Outline each Plasmodium falciparum-infected red blood cell.
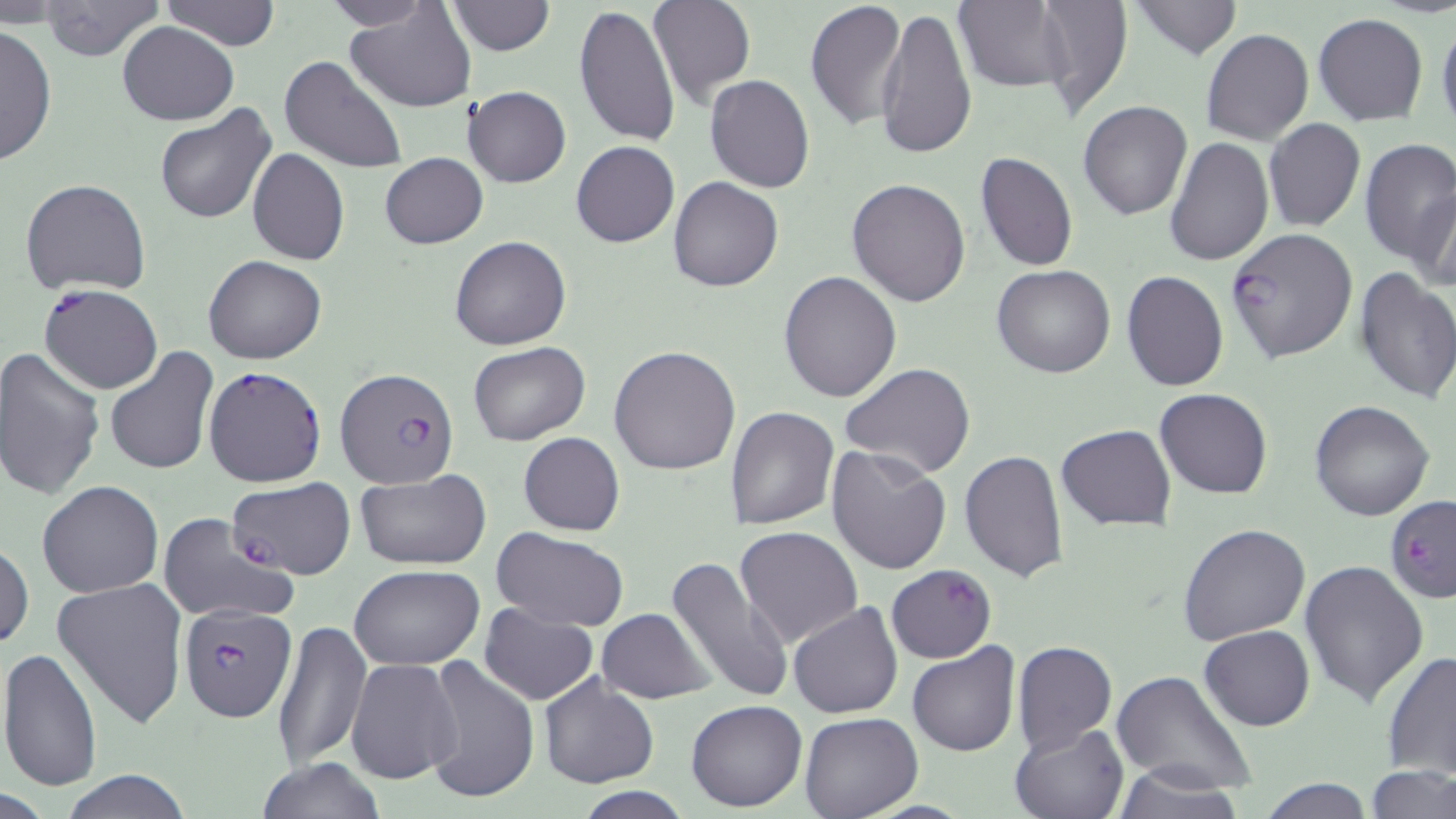

Approximate bounding boxes as (x1,y1)-(x2,y2) corner pairs in pixels.
Plasmodium falciparum-infected red blood cells: (1225,229)-(1358,364), (39,283)-(163,394), (203,367)-(326,486), (334,367)-(459,489), (228,476)-(355,582), (1384,495)-(1456,604), (887,565)-(997,663), (179,603)-(298,722).

slide_level_diagnosis: Plasmodium falciparum
image_size: 1456×819 pixels
stain: May-Grünwald-Giemsa
preparation: thin blood film
magnification: 1000x
uninfected_red_blood_cell_locations: 'approximate bounding boxes as (x1,y1)-(x2,y2) corner pairs in pixels: (160,0)-(281,50), (319,0)-(435,30), (803,0)-(908,131), (1035,0)-(1133,116), (1127,0)-(1243,60), (36,1)-(165,61), (446,1)-(555,55), (647,1)-(756,109), (343,2)-(477,113), (956,2)-(1073,92), (55,5)-(225,83), (574,5)-(680,147), (875,5)-(976,160), (1313,12)-(1428,125), (1437,20)-(1456,128), (117,21)-(238,125), (0,23)-(56,167), (1202,30)-(1313,144), (279,53)-(407,174), (706,75)-(815,192), (462,86)-(570,188), (1078,100)-(1193,220), (153,104)-(276,225), (1263,119)-(1365,233), (1163,136)-(1273,266), (1358,137)-(1455,265), (571,141)-(678,249), (247,148)-(348,265), (976,152)-(1077,273), (379,153)-(487,249), (668,176)-(784,292), (20,177)-(151,296), (845,177)-(972,307), (1414,182)-(1456,294), (449,237)-(571,351), (203,254)-(326,364), (991,265)-(1116,379), (1353,266)-(1456,404), (777,270)-(901,404), (1122,271)-(1228,391), (468,342)-(590,447), (103,346)-(220,475), (609,346)-(740,475), (0,348)-(105,500), (841,363)-(975,480), (1155,388)-(1272,498), (1309,399)-(1434,521), (725,407)-(840,531), (1057,425)-(1175,530), (518,432)-(624,535), (825,444)-(952,575), (958,449)-(1069,581), (354,471)-(491,568), (37,480)-(164,598), (155,514)-(297,626), (1178,524)-(1311,646), (734,525)-(863,650), (492,528)-(628,633), (0,541)-(34,652), (663,555)-(796,706), (1298,560)-(1429,707), (351,565)-(484,670), (52,577)-(189,729), (788,602)-(904,718), (479,605)-(598,705), (595,608)-(715,704), (272,620)-(371,772), (1198,625)-(1315,731), (1011,641)-(1116,755), (907,642)-(1021,757), (0,646)-(104,793), (1381,649)-(1456,779), (422,656)-(539,805), (345,657)-(462,785), (1110,670)-(1258,797), (537,672)-(659,789), (686,699)-(807,813), (799,712)-(923,819), (1009,722)-(1129,818), (254,757)-(388,818), (1112,766)-(1250,819), (1365,767)-(1456,819), (59,770)-(196,818), (1255,778)-(1377,817), (569,788)-(695,818)'
field_of_view: one of a larger specimen
modality: optical microscopy